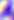
Summary:
  - Magnification: 400x
  - Modality: micrograph
  - Identification: Toxoplasma gondii